State which parasite is depicted.
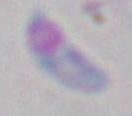
This is Toxoplasma gondii.

Summary:
  - Modality: photomicrograph
  - Magnification: 1000x